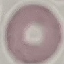

malaria status = uninfected
preparation = thin smear
image type = cell patch, automatically extracted from a larger field of view and resized to 64 × 64 pixels
capture = smartphone camera at the microscope eyepiece
stain = Giemsa